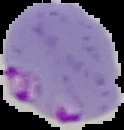
image size = 124×130 pixels
result = malaria parasites detected
preparation = thin blood film
image type = cell region segmented out of the field of view; surrounding area masked to black